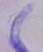
Micrograph. A trypanosome is shown. 1000x magnification.